Mark where cells are.
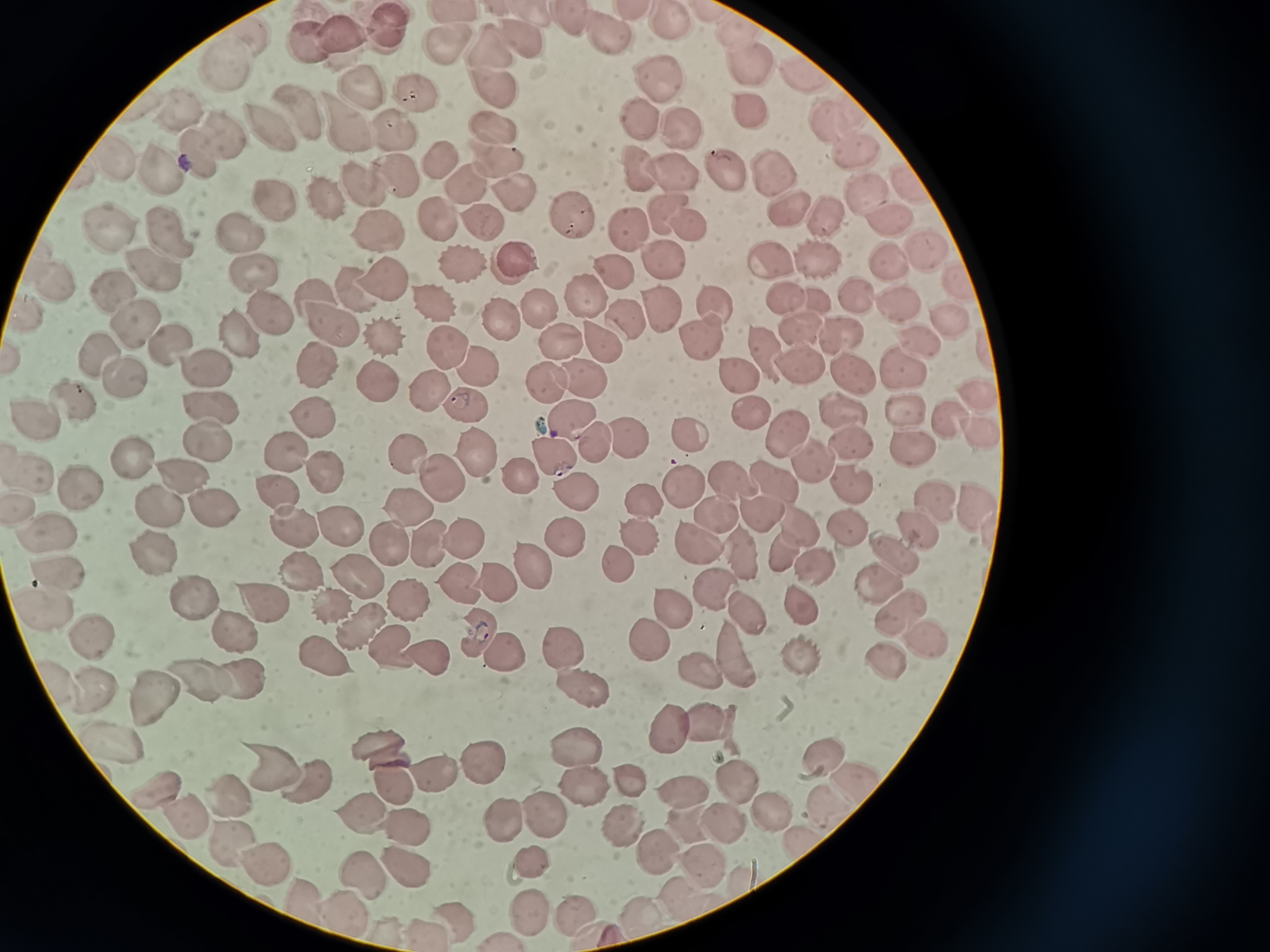

Approximate centers as (x, y) in pixels.
Cells: (452, 15), (320, 17), (574, 24), (673, 24), (741, 27), (256, 32), (390, 32), (342, 36), (609, 36), (524, 38), (311, 44), (444, 48), (494, 49), (231, 62), (750, 64), (809, 73), (663, 80), (356, 85), (491, 85), (410, 90), (297, 110), (182, 112), (753, 113), (842, 115), (631, 117), (266, 123), (496, 127), (395, 130), (349, 131), (679, 131), (223, 132), (857, 155), (444, 157), (198, 158), (499, 158), (113, 162), (161, 171), (734, 171), (640, 172), (395, 177), (775, 177), (676, 178), (364, 182), (904, 185), (468, 188), (874, 194), (515, 195), (322, 196), (273, 197), (665, 211), (797, 211), (835, 214), (573, 215), (441, 220), (887, 220), (487, 221), (110, 224), (694, 224), (373, 231), (625, 231), (166, 233), (241, 233), (927, 250), (663, 257), (769, 257), (819, 259), (890, 261), (458, 263), (513, 263), (147, 273), (614, 274), (256, 275), (383, 278), (953, 283), (60, 284), (109, 285), (355, 289), (856, 291), (311, 293), (584, 295), (779, 298), (895, 301), (429, 302), (28, 304), (275, 307), (714, 308), (540, 311), (660, 314), (627, 318), (501, 320), (945, 320), (134, 321), (333, 328), (799, 329), (841, 333), (238, 335), (388, 339), (562, 340), (922, 341), (173, 342), (700, 342), (604, 345), (452, 348), (101, 350), (761, 356), (312, 364), (796, 365), (908, 366), (482, 368), (209, 371), (732, 372), (130, 374), (579, 378), (858, 378), (370, 380), (543, 382), (431, 389), (979, 394), (74, 403), (837, 403), (472, 404), (900, 406), (217, 411), (749, 412), (946, 416), (570, 417), (317, 420), (46, 421), (783, 429), (626, 435), (692, 435), (980, 435), (849, 440), (211, 441), (589, 444), (914, 446), (138, 453), (295, 453), (412, 455), (480, 455), (815, 457), (553, 458), (178, 473), (331, 473), (34, 474), (526, 477), (727, 479), (777, 479), (442, 480), (853, 481), (683, 484), (85, 490), (279, 490), (576, 493), (642, 498), (935, 502), (407, 503), (216, 505), (979, 507), (156, 509), (718, 516), (761, 516), (798, 525), (844, 526), (296, 528), (345, 528), (919, 528), (54, 532), (564, 535), (459, 536), (635, 536), (693, 544), (396, 545), (781, 546), (152, 552), (893, 553), (615, 562), (530, 564), (820, 568), (66, 571), (301, 573), (359, 576), (877, 577), (455, 582), (494, 582), (713, 589), (187, 595), (409, 595), (262, 599), (334, 602), (664, 605), (39, 608), (901, 608), (742, 609), (800, 612), (362, 631), (235, 632), (89, 634), (477, 636), (648, 637), (929, 637), (391, 647), (561, 649), (806, 651), (725, 652), (318, 654), (428, 654), (504, 655), (892, 663), (695, 666), (237, 676), (191, 678), (582, 689), (98, 693), (148, 699), (711, 718), (673, 731), (111, 739), (380, 745), (576, 748), (822, 751), (483, 755), (272, 766), (437, 776), (635, 779), (582, 780), (733, 780), (307, 783), (393, 784), (856, 784), (160, 788), (678, 788), (232, 793), (773, 809), (543, 811), (362, 812), (184, 815), (510, 818), (725, 821), (688, 822), (401, 829), (232, 844), (658, 850), (706, 858), (532, 865), (267, 866), (363, 870), (401, 870), (679, 889), (312, 905), (636, 909), (525, 910), (578, 910), (350, 914), (451, 915), (424, 929).

image size = 1270×952 pixels
preparation = thin smear
capture = smartphone camera at the microscope eyepiece
field of view = single
stain = Giemsa